Assess the morphology of the erythrocytes.
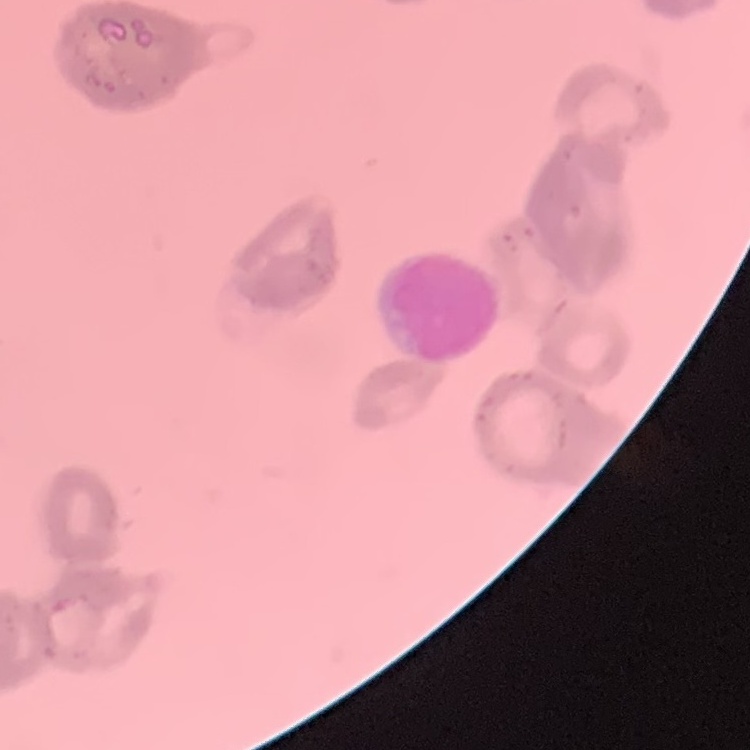
They show rouleaux formation.

preparation = thin blood smear
stain = Field's or Giemsa
image type = square crop of a larger photomicrograph